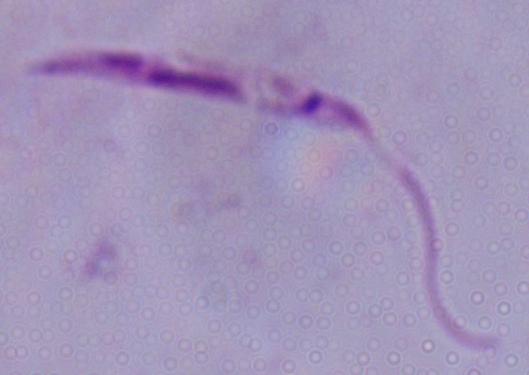

identification = Leishmania
modality = micrograph
magnification = 1000x